State which parasite is depicted.
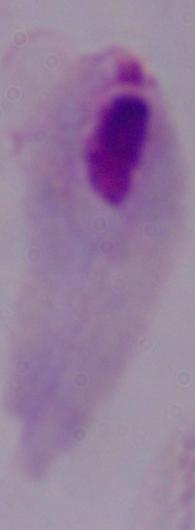

This is a trichomonad.

modality = photomicrograph
magnification = 1000x